Assess the morphology of the red blood cells.
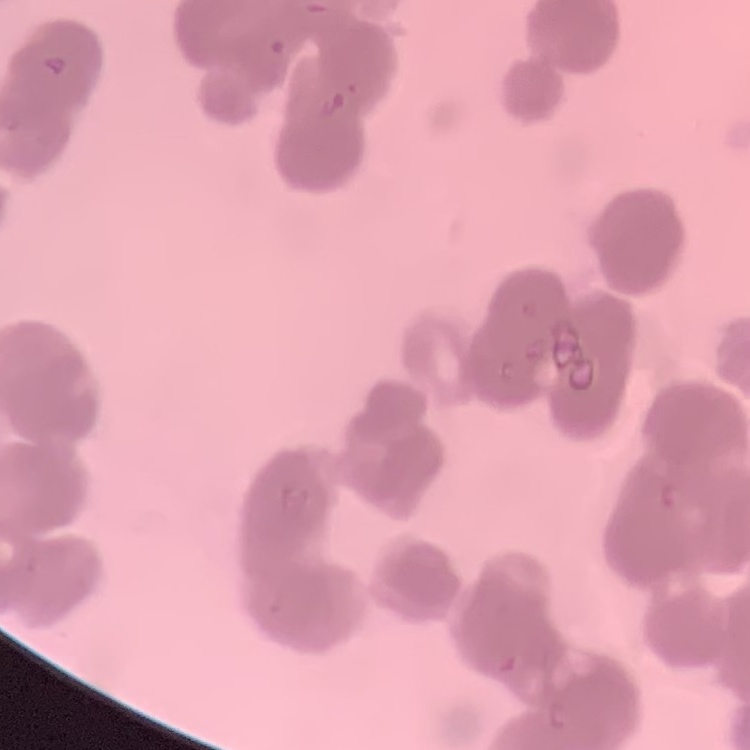

They show rouleaux formation.

image type = one tile cut from a larger photomicrograph
stain = Field's or Giemsa
preparation = thin peripheral smear